Give the extent of all Plasmodium ovale-infected red blood cells.
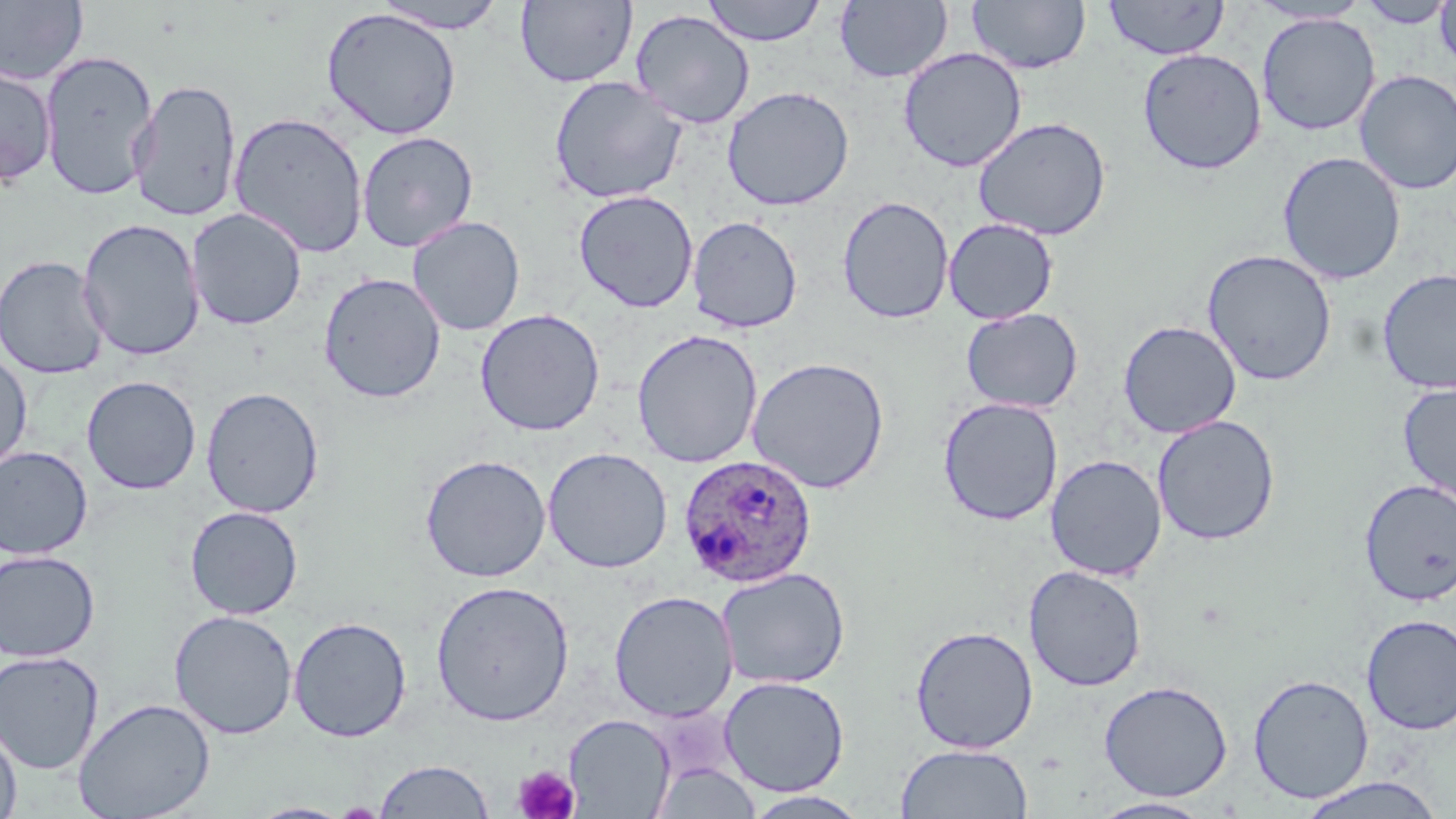

Approximate bounding boxes as [x1, y1, x2, y2] in pixels.
Plasmodium ovale-infected red blood cells: [677, 453, 817, 589].

Summary:
  - Uninfected red blood cell locations: [515, 0, 637, 88], [702, 0, 826, 46], [835, 0, 952, 84], [967, 0, 1091, 75], [1103, 0, 1229, 61], [0, 1, 88, 85], [370, 1, 510, 34], [1356, 1, 1454, 28], [1434, 1, 1456, 73], [1249, 2, 1372, 25], [321, 6, 462, 141], [629, 9, 756, 129], [1256, 13, 1380, 135], [898, 47, 1027, 172], [1137, 48, 1267, 175], [39, 49, 158, 201], [0, 62, 57, 187], [1354, 69, 1456, 195], [548, 75, 688, 204], [129, 79, 242, 222], [721, 86, 855, 211], [228, 111, 369, 259], [972, 116, 1112, 241], [356, 131, 479, 252], [1277, 151, 1406, 285], [574, 189, 699, 313], [837, 195, 955, 324], [186, 207, 307, 331], [687, 215, 803, 333], [407, 216, 525, 336], [77, 218, 206, 360], [943, 218, 1058, 324], [1202, 249, 1337, 386], [0, 255, 110, 380], [1377, 267, 1456, 395], [318, 272, 446, 404], [961, 307, 1083, 413], [475, 308, 606, 437], [1118, 320, 1241, 438], [630, 328, 764, 468], [0, 349, 33, 477], [747, 357, 890, 494], [81, 375, 201, 494], [1397, 382, 1456, 504], [200, 386, 324, 518], [938, 397, 1064, 526], [1151, 415, 1280, 545], [0, 446, 94, 560], [542, 447, 673, 573], [420, 454, 551, 583], [1045, 454, 1167, 581], [1358, 479, 1456, 606], [184, 505, 304, 619], [0, 550, 100, 662], [1023, 565, 1147, 692], [716, 566, 851, 689], [430, 579, 575, 726], [608, 589, 739, 722], [169, 609, 298, 740], [1360, 614, 1456, 735], [288, 616, 412, 742], [910, 625, 1039, 754], [0, 651, 104, 775], [1247, 674, 1374, 803], [718, 675, 850, 795], [1098, 679, 1233, 801], [73, 697, 215, 819], [563, 713, 675, 818], [0, 719, 22, 819], [895, 743, 1033, 818], [374, 759, 494, 818], [651, 760, 762, 819], [1297, 775, 1447, 818], [742, 790, 872, 818], [1089, 796, 1216, 818], [249, 802, 354, 819]
  - Platelet locations: [512, 764, 580, 818]
  - Slide-level diagnosis: Plasmodium ovale
  - Field of view: one of a larger specimen
  - Stain: May-Grünwald-Giemsa
  - Preparation: thin blood smear
  - Image size: 1456×819 pixels
  - Magnification: 1000x
  - Modality: optical microscopy